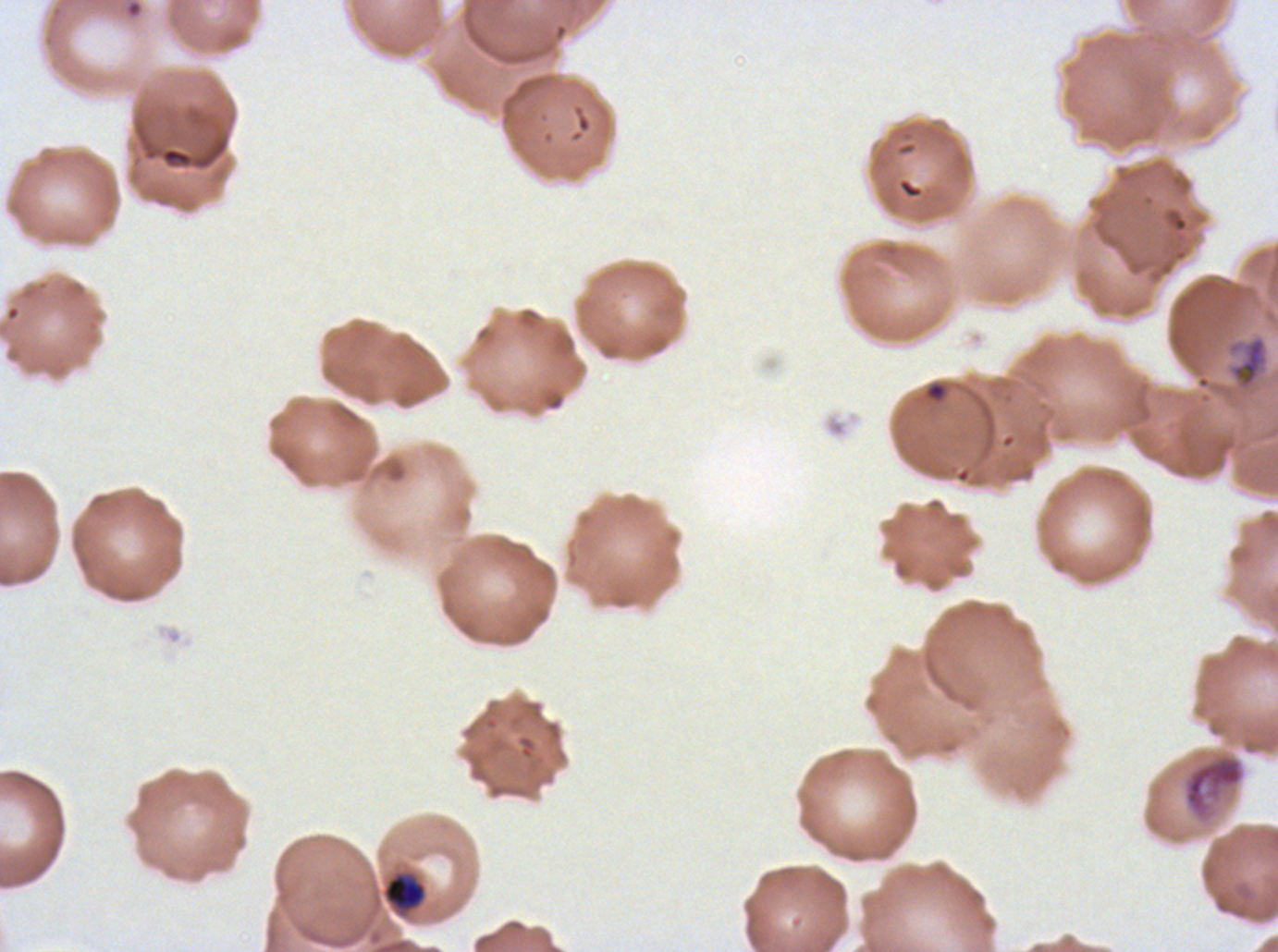

Approximate bounding boxes as [x1, y1, x2, y2] in pixels. Late-ring/early-trophozoite locations: [383, 873, 425, 910]. Debris locations: [160, 146, 193, 168], [1181, 751, 1247, 826]. Mid trophozoite locations: [1225, 335, 1270, 393]. Life-cycle stages observed: late-ring/early-trophozoite, mid trophozoite. Giemsa stain. Plasmodium falciparum from a patient in The Gambia, cultured ex vivo for 24 to 48 hours. Image is 1278×952 pixels. Thin blood smear. A sub-image separated from a larger composite.